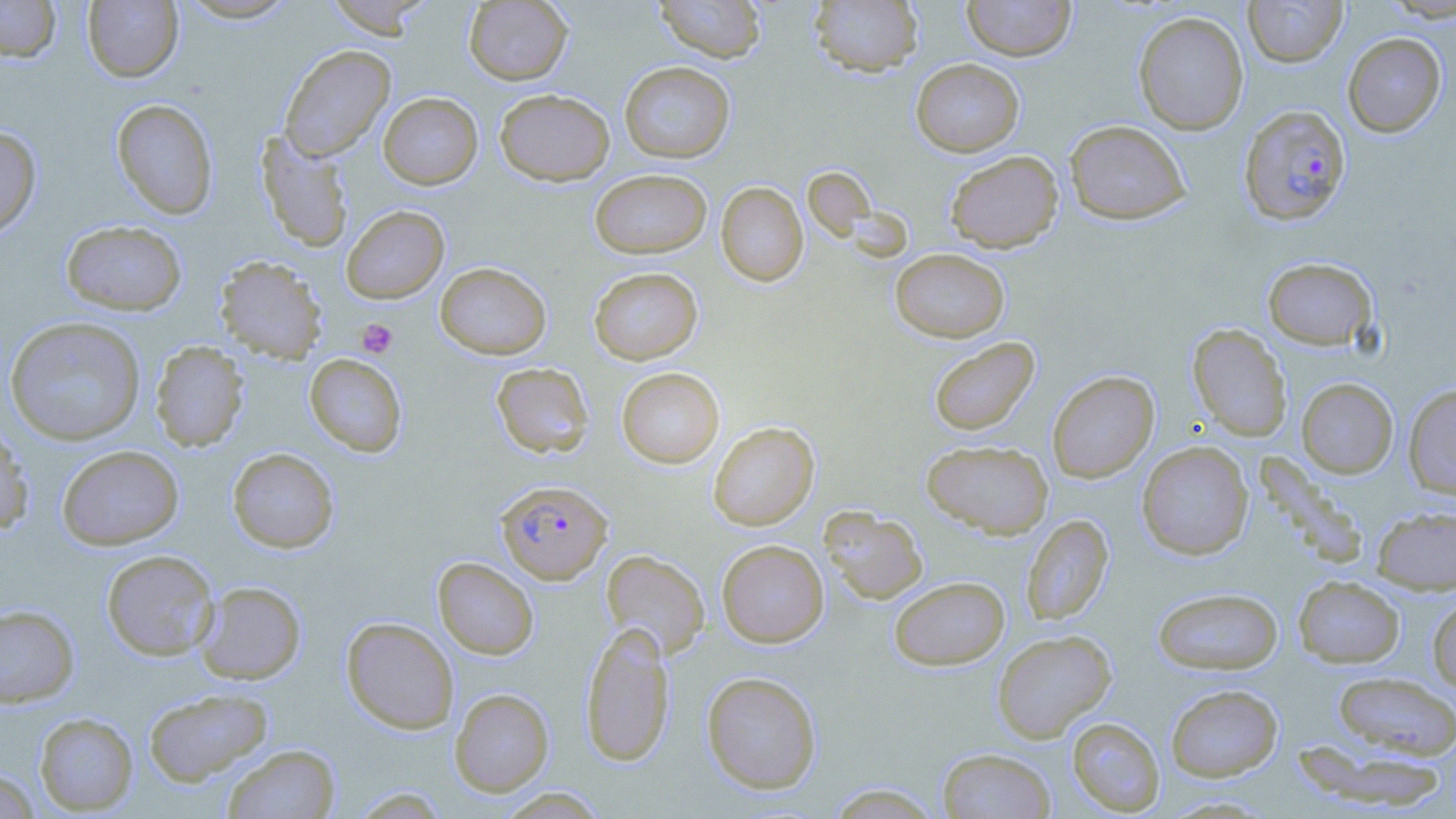
{
  "plasmodium_falciparum_infected_red_blood_cell_locations": "approximate bounding boxes as named x1/y1/x2/y2 corners in pixels: (x1=1238, y1=105, x2=1352, y2=226), (x1=496, y1=480, x2=613, y2=584)",
  "slide_level_diagnosis": "Plasmodium falciparum",
  "preparation": "thin blood smear",
  "modality": "optical microscopy",
  "magnification": "1000x",
  "platelet_locations": "approximate bounding boxes as named x1/y1/x2/y2 corners in pixels: (x1=357, y1=318, x2=398, y2=358)",
  "field_of_view": "one of a larger specimen",
  "image_size": "1456×819 pixels",
  "stain": "May-Grünwald-Giemsa",
  "uninfected_red_blood_cell_locations": "approximate bounding boxes as named x1/y1/x2/y2 corners in pixels: (x1=0, y1=0, x2=62, y2=63), (x1=175, y1=0, x2=302, y2=23), (x1=322, y1=0, x2=436, y2=38), (x1=464, y1=0, x2=572, y2=85), (x1=653, y1=0, x2=766, y2=63), (x1=809, y1=0, x2=924, y2=77), (x1=962, y1=0, x2=1076, y2=61), (x1=1243, y1=0, x2=1347, y2=67), (x1=1380, y1=0, x2=1456, y2=23), (x1=82, y1=1, x2=183, y2=82), (x1=1133, y1=11, x2=1249, y2=135), (x1=1342, y1=32, x2=1447, y2=137), (x1=279, y1=45, x2=396, y2=162), (x1=910, y1=58, x2=1024, y2=157), (x1=619, y1=61, x2=736, y2=163), (x1=495, y1=88, x2=615, y2=186), (x1=378, y1=92, x2=483, y2=189), (x1=111, y1=98, x2=219, y2=219), (x1=1064, y1=120, x2=1191, y2=225), (x1=0, y1=125, x2=42, y2=240), (x1=255, y1=131, x2=353, y2=252), (x1=944, y1=150, x2=1064, y2=253), (x1=802, y1=166, x2=877, y2=241), (x1=590, y1=168, x2=712, y2=259), (x1=716, y1=181, x2=808, y2=287), (x1=341, y1=205, x2=449, y2=304), (x1=60, y1=220, x2=188, y2=316), (x1=890, y1=248, x2=1010, y2=343), (x1=214, y1=256, x2=328, y2=365), (x1=1262, y1=257, x2=1379, y2=351), (x1=435, y1=262, x2=552, y2=360), (x1=589, y1=266, x2=703, y2=365), (x1=4, y1=316, x2=147, y2=446), (x1=1187, y1=324, x2=1292, y2=442), (x1=927, y1=336, x2=1040, y2=437), (x1=150, y1=341, x2=250, y2=452), (x1=304, y1=353, x2=408, y2=457), (x1=491, y1=362, x2=594, y2=458), (x1=616, y1=367, x2=725, y2=468), (x1=1047, y1=370, x2=1159, y2=483), (x1=1296, y1=378, x2=1398, y2=478), (x1=1403, y1=383, x2=1456, y2=499), (x1=707, y1=421, x2=819, y2=531), (x1=0, y1=425, x2=35, y2=536), (x1=921, y1=439, x2=1053, y2=539), (x1=1137, y1=441, x2=1253, y2=560), (x1=56, y1=444, x2=184, y2=550), (x1=227, y1=447, x2=339, y2=553), (x1=1372, y1=505, x2=1456, y2=593), (x1=821, y1=507, x2=928, y2=605), (x1=1021, y1=514, x2=1113, y2=625), (x1=716, y1=539, x2=829, y2=647), (x1=101, y1=549, x2=219, y2=660), (x1=601, y1=549, x2=710, y2=660), (x1=433, y1=557, x2=539, y2=659), (x1=889, y1=576, x2=1010, y2=670), (x1=1293, y1=576, x2=1405, y2=668), (x1=194, y1=581, x2=306, y2=684), (x1=1152, y1=586, x2=1284, y2=675), (x1=1427, y1=595, x2=1456, y2=693), (x1=0, y1=604, x2=79, y2=708), (x1=341, y1=616, x2=459, y2=734), (x1=579, y1=622, x2=675, y2=767), (x1=992, y1=630, x2=1116, y2=743), (x1=701, y1=670, x2=822, y2=794), (x1=1331, y1=671, x2=1456, y2=760), (x1=1165, y1=683, x2=1283, y2=781), (x1=142, y1=687, x2=273, y2=787), (x1=449, y1=688, x2=554, y2=796), (x1=34, y1=712, x2=139, y2=815), (x1=1066, y1=717, x2=1165, y2=816), (x1=223, y1=744, x2=340, y2=819), (x1=937, y1=747, x2=1056, y2=818), (x1=0, y1=768, x2=42, y2=818), (x1=825, y1=783, x2=947, y2=819), (x1=495, y1=787, x2=609, y2=818)"
}